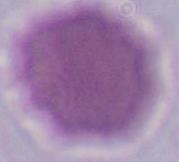

Photomicrograph. 1000x magnification. An erythrocyte is shown.